Describe the morphology of the erythrocytes.
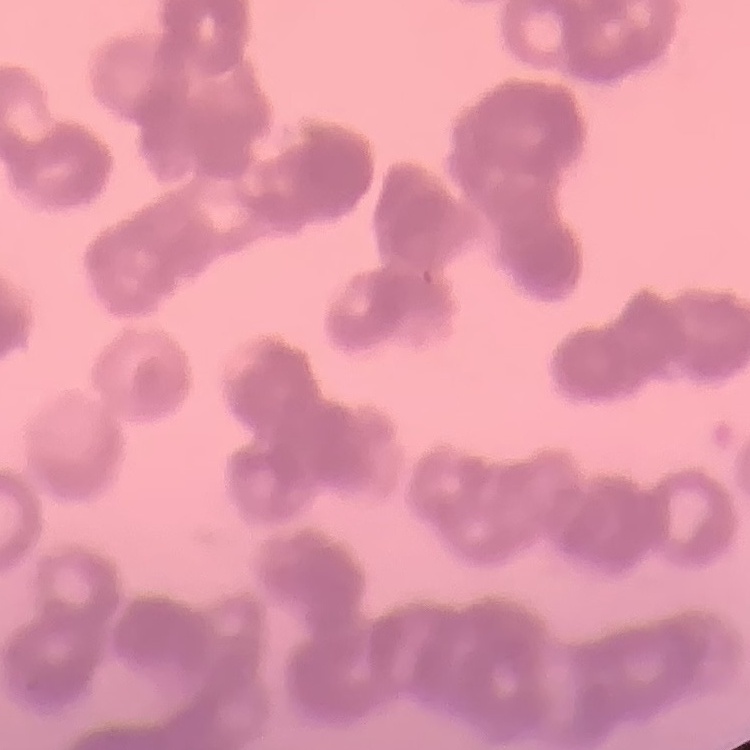
They show rouleaux formation.

Summary:
  - Preparation: thin peripheral smear
  - Image type: one tile cut from a larger photomicrograph
  - Stain: Field's or Giemsa